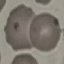 Malaria status: uninfected. Automatically extracted cell patch, resized to 64 × 64 pixels. Photographed with a smartphone camera at the microscope eyepiece. Giemsa-stained preparation. Thin blood smear.